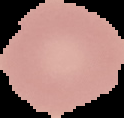

Summary:
  - Image type: segmented cell region on a black background
  - Image size: 124×118 pixels
  - Preparation: thin blood smear
  - Result: no Plasmodium parasites seen